Assess this cell for malaria.
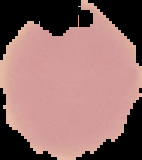

It is uninfected.

Summary:
  - Preparation: thin blood smear
  - Image type: segmented cell region on a black background
  - Image size: 142×160 pixels